Classify this cell by malaria status.
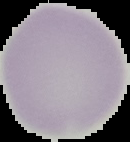
It is uninfected.

Segmented cell region on a black background. From a thin blood smear. Image is 130×142 pixels.